Identify the parasite.
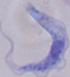
A trypanosome.

{
  "modality": "photomicrograph",
  "magnification": "1000x"
}